Classify this cell by malaria status.
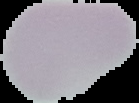
Uninfected.

Summary:
  - Image size: 139×103 pixels
  - Image type: segmented cell region with the area outside set to black
  - Preparation: thin blood smear